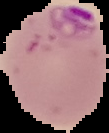

Summary:
  - Image size: 109×133 pixels
  - Result: malaria parasites identified
  - Preparation: thin blood smear
  - Image type: cell region segmented out of the field of view; surrounding area masked to black